Identify the blood parasite species.
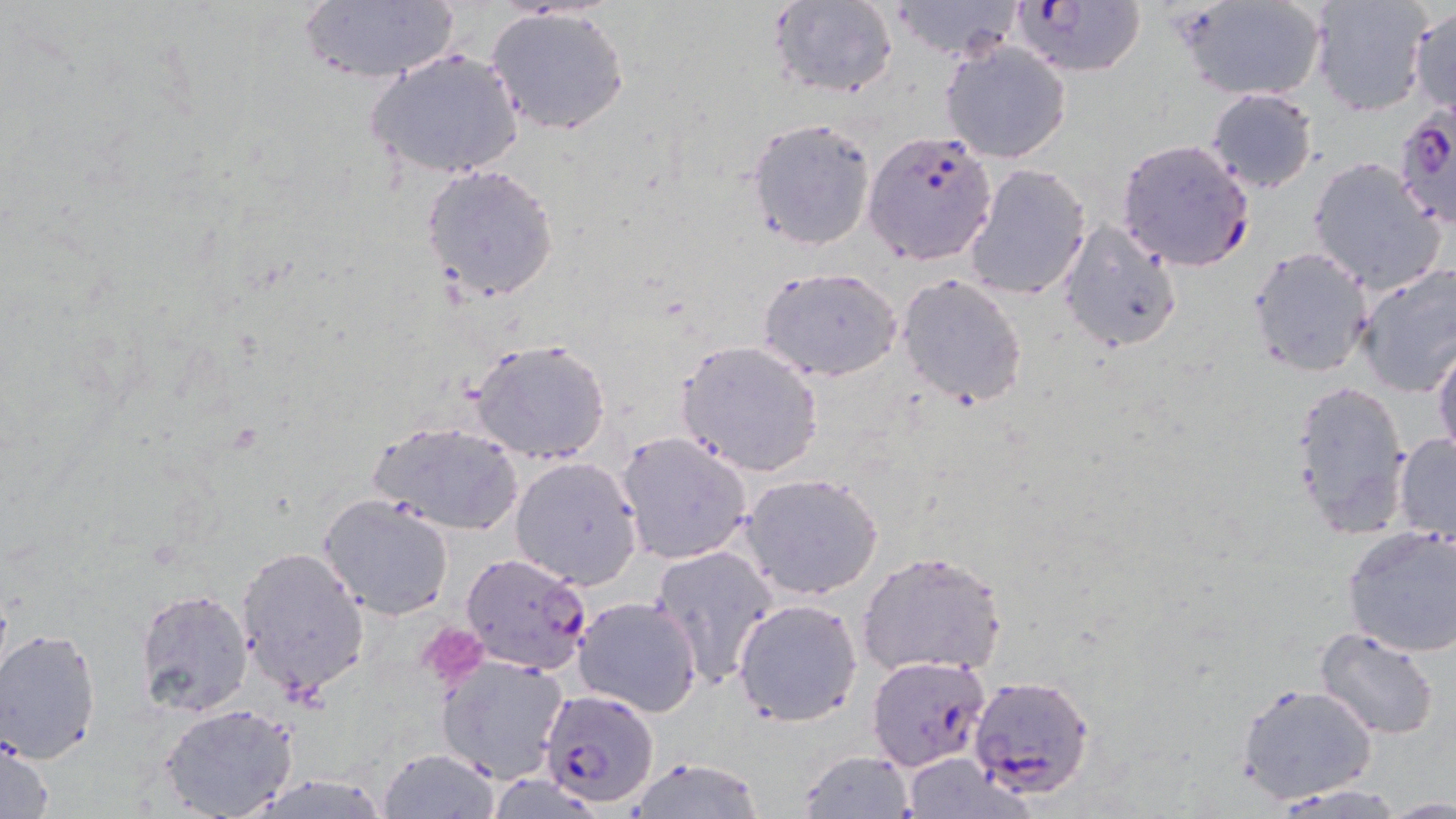

Plasmodium falciparum.

Approximate bounding boxes as (x1,y1)-(x2,y2) corner pairs in pixels. Uninfected red blood cell locations: (765,0)-(900,100), (884,0)-(1025,64), (1181,0)-(1328,101), (1309,0)-(1433,117), (296,2)-(462,85), (484,5)-(632,136), (1407,5)-(1456,118), (940,41)-(1071,163), (366,45)-(525,180), (1205,87)-(1319,194), (745,117)-(877,250), (1306,156)-(1449,295), (421,162)-(560,303), (961,162)-(1093,302), (1057,221)-(1183,353), (1246,245)-(1374,378), (1353,263)-(1456,398), (757,264)-(902,382), (896,271)-(1029,408), (470,338)-(613,465), (675,339)-(824,477), (1431,339)-(1456,467), (1289,376)-(1413,538), (368,418)-(525,536), (616,431)-(753,565), (1393,432)-(1456,542), (509,456)-(643,590), (740,472)-(884,600), (319,493)-(456,620), (1341,524)-(1456,657), (649,544)-(778,686), (235,545)-(369,697), (856,549)-(1008,678), (136,587)-(255,715), (573,595)-(704,716), (733,597)-(861,725), (1313,628)-(1441,741), (0,630)-(102,764), (1265,642)-(1407,771), (435,653)-(570,786), (1235,681)-(1378,806), (158,702)-(298,818), (1,733)-(55,818), (378,748)-(502,818), (797,749)-(915,819), (898,755)-(1025,819), (624,757)-(767,818), (1269,782)-(1410,817), (1385,794)-(1455,817). Plasmodium falciparum-infected red blood cell locations: (1010,0)-(1145,79), (1391,106)-(1456,233), (864,130)-(997,266), (1116,138)-(1257,272), (459,551)-(592,676), (868,655)-(991,772), (968,672)-(1095,798), (538,687)-(661,806). Platelet locations: (415,621)-(488,690). May-Grünwald-Giemsa-stained preparation. Light microscopy. One field of a larger specimen. Thin blood smear. 1000x magnification. Image is 1456×819 pixels.